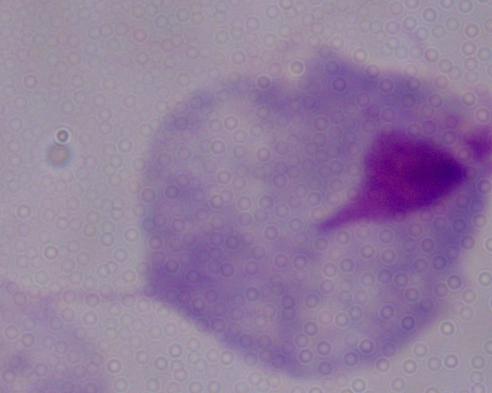
Summary:
  - Magnification: 1000x
  - Identification: trichomonad
  - Modality: micrograph